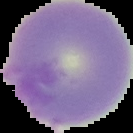
Malaria status: uninfected. Image is 133×133 pixels. The area outside the segmented cell region is set to black. From a thin blood smear.